Report the malaria status of this cell.
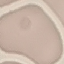

Uninfected.

Acquired by smartphone through the microscope eyepiece. Thin smear of blood. Cell patch, automatically extracted from a larger field of view and resized to 64 × 64 pixels. Giemsa stain.